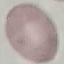
result: no malaria parasites seen
capture: smartphone camera at the microscope eyepiece
preparation: thin smear
stain: Giemsa
image_type: cell patch, automatically extracted from a larger field of view and resized to 64 × 64 pixels